Identify the preparation type.
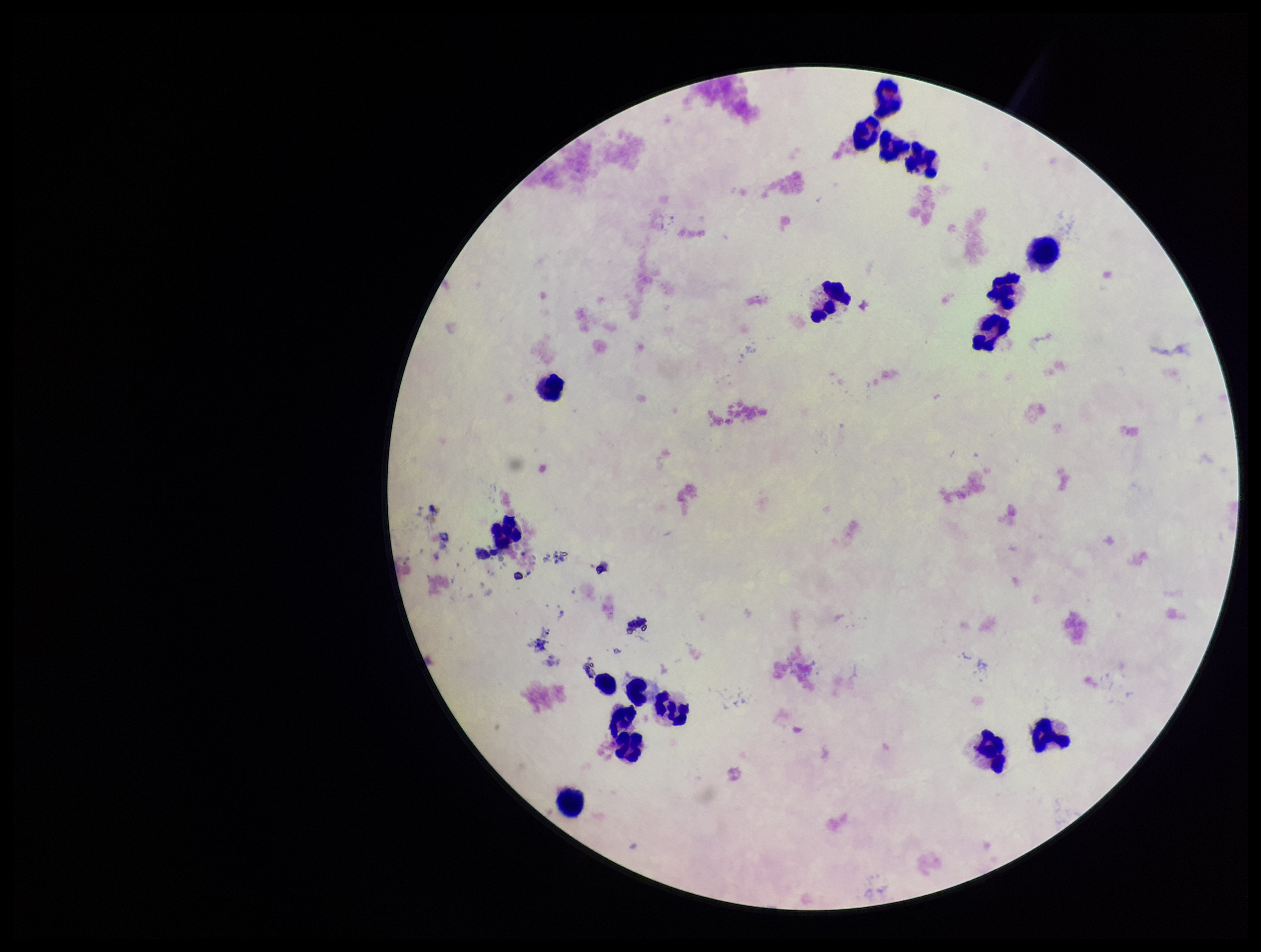

It is a thick blood smear.

Summary:
  - Plasmodium parasites: none identified
  - Parasite count: 0
  - Stain: Giemsa
  - Leukocyte count: 17
  - Field of view: single
  - Image size: 1261×952 pixels
  - Capture: smartphone photograph through the microscope eyepiece
  - Patient malaria status: negative